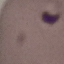

Summary:
  - Result: no malaria parasites seen
  - Image type: automatically extracted cell patch, resized to 64 × 64 pixels
  - Stain: Giemsa
  - Preparation: thin blood film
  - Capture: smartphone through the microscope eyepiece